Assess the morphology of the red blood cells.
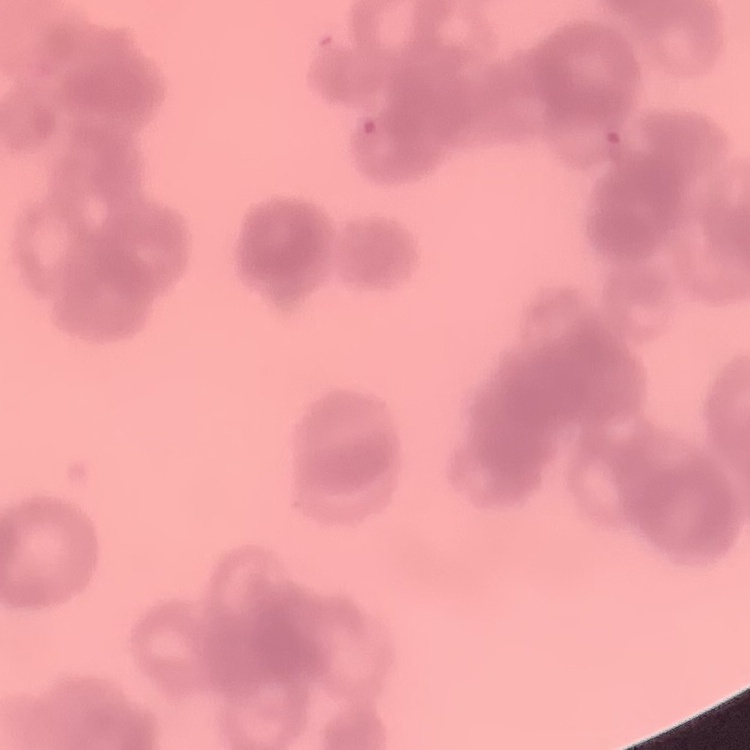
They show rouleaux formation.

Field's or Giemsa stain. One tile cut from a larger photomicrograph. Thin peripheral smear.